Name the blood parasite species.
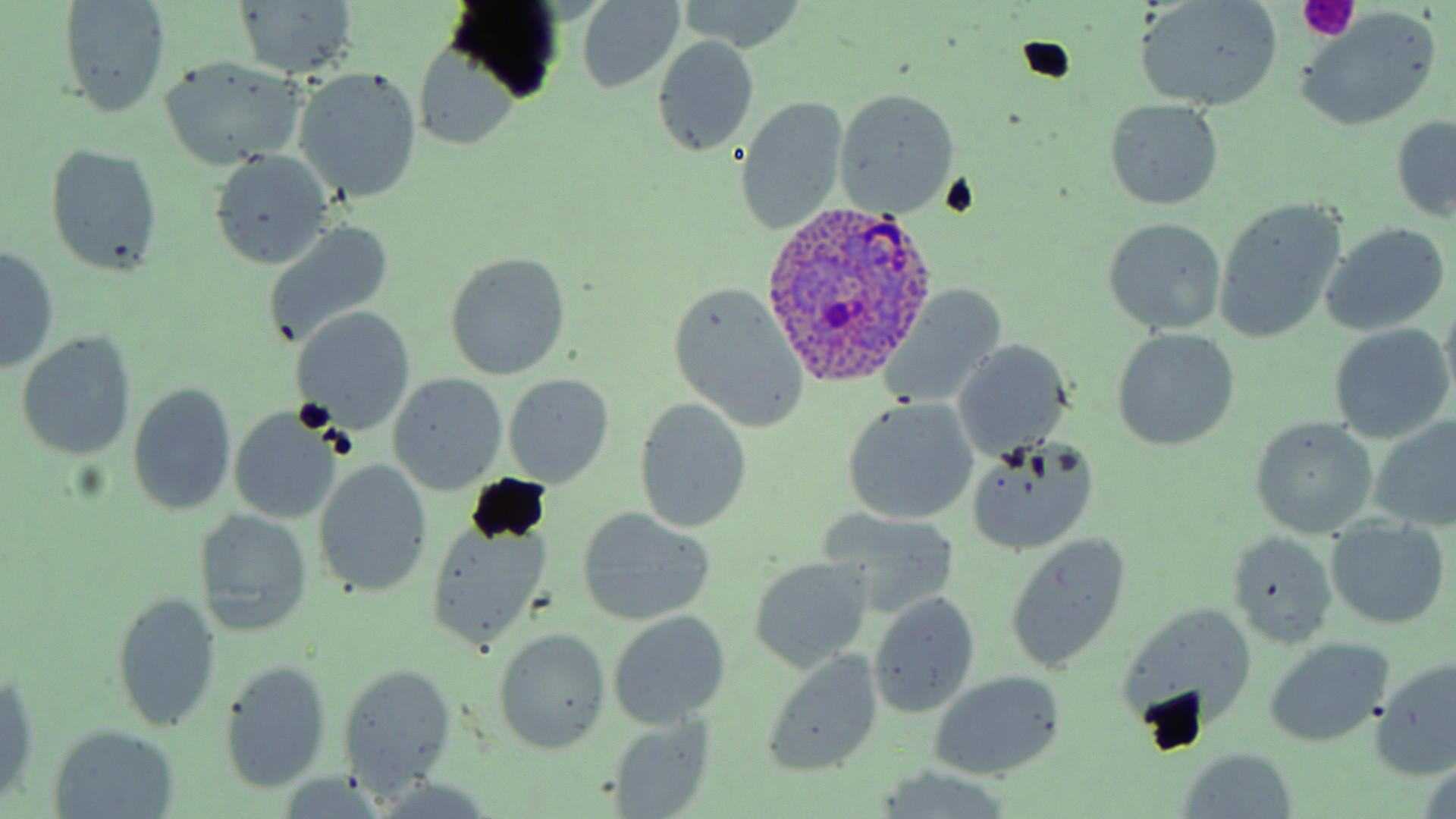

Plasmodium ovale.

field of view = one of a larger specimen
modality = optical microscopy
Plasmodium ovale-infected red blood cell locations = approximate bounding boxes as [x1, y1, x2, y2] in pixels: [757, 196, 937, 388]
image size = 1456×819 pixels
preparation = thin blood film
platelet locations = approximate bounding boxes as [x1, y1, x2, y2] in pixels: [1298, 0, 1361, 43]
magnification = 1000x
stain = May-Grünwald-Giemsa
uninfected red blood cell locations = approximate bounding boxes as [x1, y1, x2, y2] in pixels: [56, 0, 173, 119], [1135, 0, 1283, 112], [229, 1, 360, 81], [574, 1, 686, 92], [675, 1, 808, 53], [1293, 13, 1442, 131], [652, 36, 761, 157], [412, 41, 523, 152], [156, 56, 307, 170], [293, 65, 423, 202], [833, 89, 960, 216], [736, 97, 850, 235], [1103, 100, 1225, 208], [1390, 114, 1455, 222], [44, 143, 164, 277], [208, 150, 337, 269], [1213, 200, 1347, 343], [1102, 218, 1228, 334], [263, 220, 395, 346], [1318, 223, 1451, 335], [1, 248, 60, 372], [444, 251, 571, 380], [668, 286, 813, 431], [882, 286, 1009, 407], [290, 307, 415, 434], [1327, 324, 1454, 443], [1109, 327, 1240, 453], [15, 332, 137, 462], [952, 338, 1073, 461], [387, 373, 507, 494], [503, 373, 617, 487], [128, 381, 237, 514], [842, 396, 980, 525], [633, 397, 752, 533], [228, 408, 343, 523], [1248, 415, 1377, 539], [1369, 415, 1456, 532], [963, 439, 1097, 557], [312, 460, 432, 598], [577, 507, 717, 625], [816, 507, 963, 617], [195, 508, 314, 638], [1325, 518, 1449, 631], [420, 523, 552, 654], [1224, 530, 1338, 652], [1003, 533, 1133, 672], [746, 556, 874, 673], [111, 591, 223, 735], [867, 592, 981, 718], [1115, 600, 1260, 738], [604, 611, 733, 729], [492, 628, 611, 756], [1261, 636, 1395, 748], [761, 651, 884, 777], [218, 659, 333, 793], [1373, 659, 1456, 779], [336, 663, 458, 795], [928, 670, 1065, 779], [1, 675, 41, 811], [604, 713, 716, 818], [44, 725, 182, 817], [1174, 748, 1300, 818], [870, 770, 1018, 818], [364, 778, 499, 816]